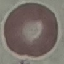

{
  "result": "no malaria parasites seen",
  "stain": "Giemsa",
  "capture": "smartphone through the microscope eyepiece",
  "image_type": "cell patch, automatically extracted from a larger field of view and resized to 64 × 64 pixels",
  "preparation": "thin smear"
}